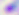 400x magnification. Photomicrograph. Toxoplasma gondii is shown.